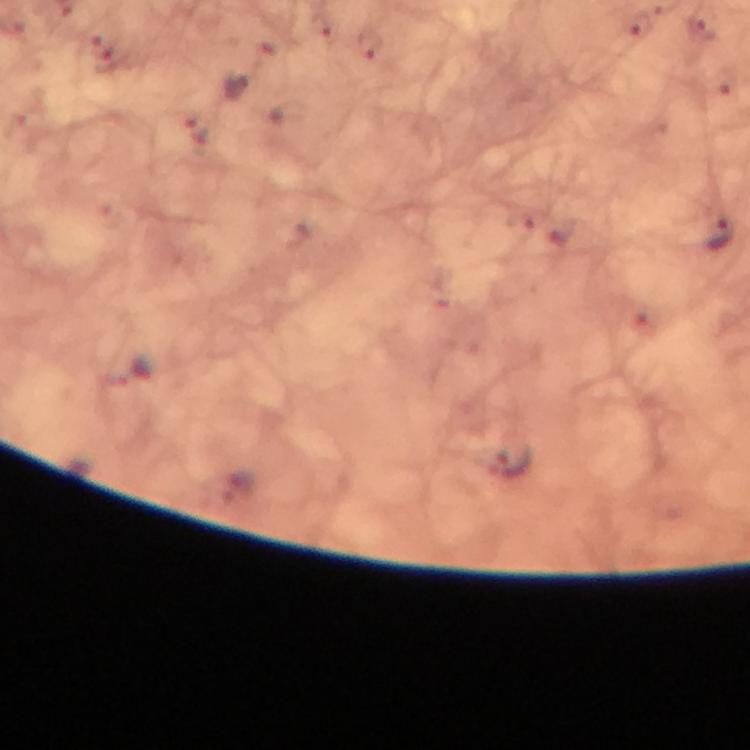
Approximate object centers, in pixels from the top-left corner.
Summary:
  - Plasmodium parasite locations: (x=640, y=24), (x=705, y=27), (x=370, y=43), (x=238, y=83), (x=198, y=130), (x=723, y=234), (x=507, y=461)
  - Context: from a diagnostic examination for malaria
  - Magnification: 100x
  - Preparation: thick blood smear
  - Immersion oil: used
  - Capture: smartphone photograph through a microscope
  - Cropped from: one field of view
  - Stain: Giemsa
  - Image size: 750×750 pixels